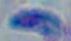 Toxoplasma gondii is seen. 1000x magnification. Photomicrograph.